Comment on the morphology of the erythrocytes.
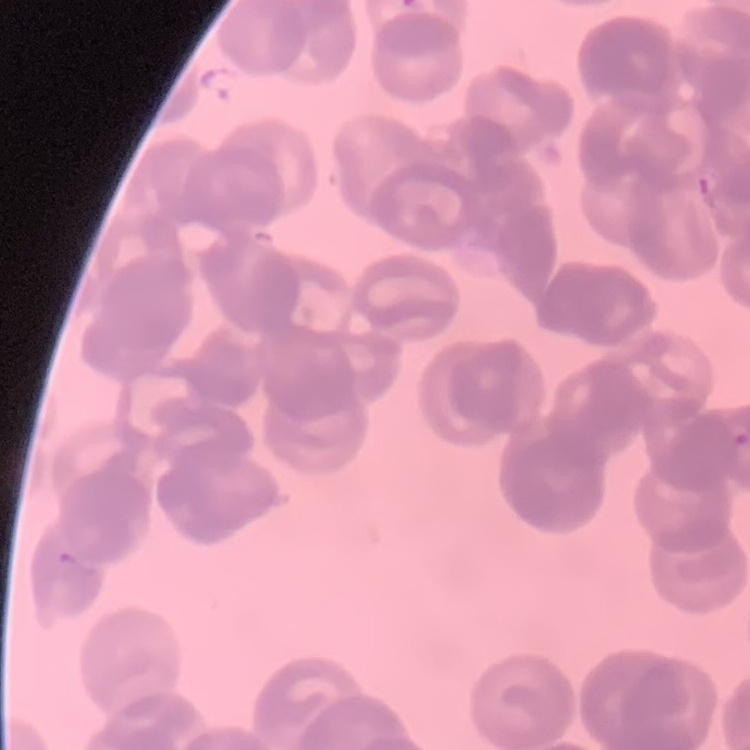

Rouleaux formation.

Summary:
  - Preparation: thin blood smear
  - Image type: one tile cut from a larger photomicrograph
  - Stain: Field's or Giemsa